Find the cells and give the type of each one.
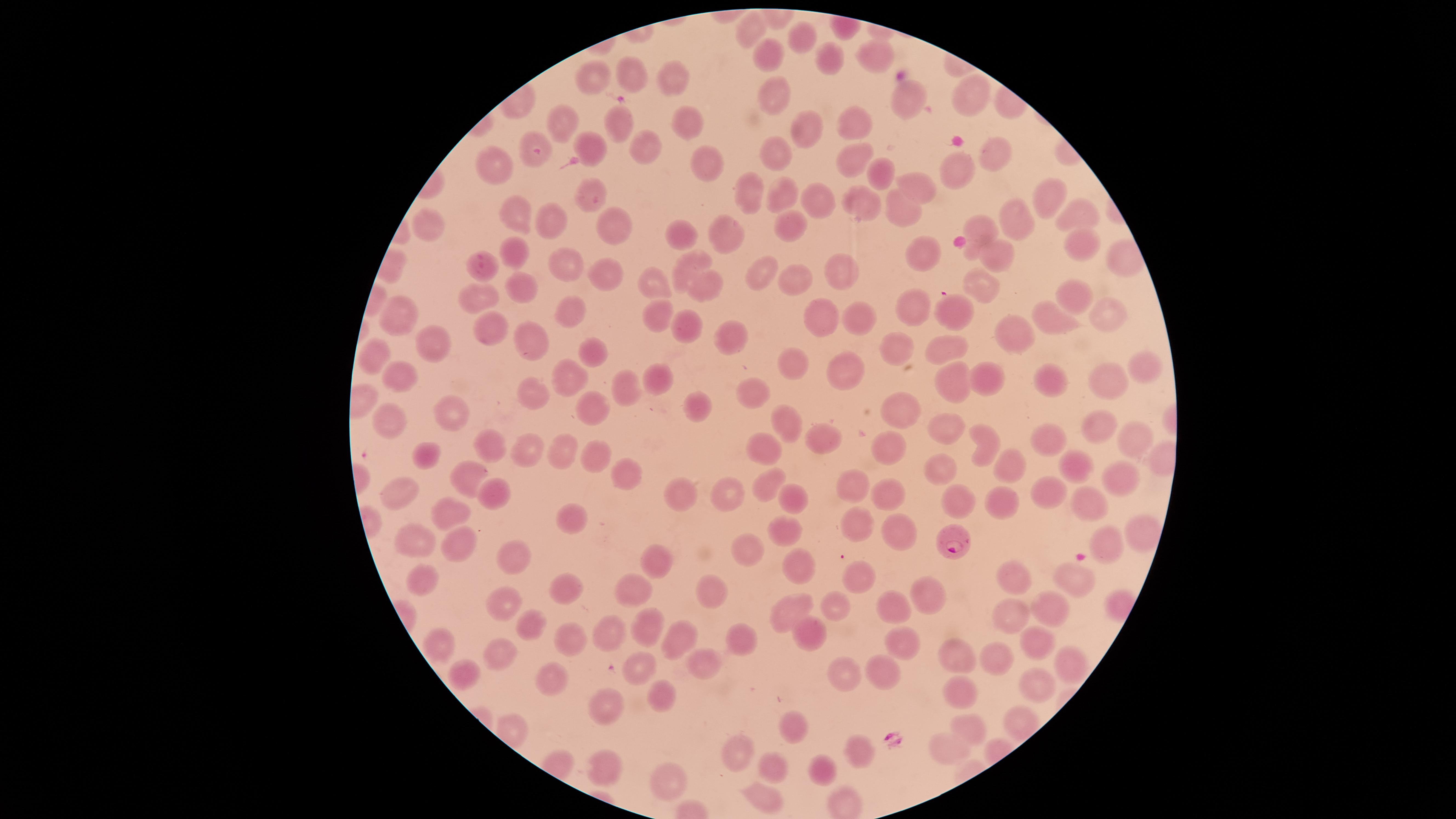

Approximate marker points as {x, y} in pixels.
Parasitized RBCs: {484, 267}, {953, 537}.
Uninfected RBCs: {752, 26}, {804, 40}, {773, 55}, {874, 55}, {829, 58}, {631, 75}, {671, 75}, {591, 77}, {774, 95}, {968, 98}, {905, 102}, {684, 118}, {564, 119}, {856, 123}, {621, 127}, {807, 130}, {531, 142}, {585, 147}, {649, 150}, {774, 153}, {990, 153}, {854, 158}, {709, 163}, {493, 166}, {876, 173}, {959, 175}, {917, 188}, {751, 194}, {1051, 194}, {591, 195}, {781, 198}, {813, 200}, {858, 200}, {900, 211}, {519, 214}, {551, 215}, {1074, 217}, {1014, 218}, {790, 222}, {428, 225}, {980, 226}, {616, 229}, {683, 230}, {723, 237}, {1077, 248}, {518, 249}, {930, 252}, {994, 254}, {560, 265}, {686, 266}, {835, 272}, {762, 274}, {606, 278}, {796, 282}, {525, 286}, {655, 286}, {982, 286}, {702, 287}, {1074, 293}, {480, 296}, {916, 308}, {566, 309}, {952, 311}, {396, 317}, {659, 317}, {818, 317}, {1110, 318}, {865, 324}, {1053, 326}, {492, 330}, {687, 330}, {1017, 332}, {727, 338}, {534, 340}, {894, 345}, {440, 347}, {947, 351}, {594, 352}, {370, 358}, {796, 362}, {848, 367}, {1144, 369}, {400, 376}, {570, 380}, {661, 381}, {984, 381}, {1047, 381}, {1111, 382}, {948, 387}, {535, 394}, {628, 395}, {752, 396}, {456, 406}, {699, 406}, {902, 407}, {397, 412}, {594, 414}, {787, 423}, {1103, 425}, {949, 427}, {825, 436}, {1050, 439}, {495, 442}, {1134, 442}, {989, 445}, {889, 448}, {766, 449}, {530, 452}, {559, 454}, {428, 457}, {590, 460}, {937, 463}, {1009, 463}, {1081, 464}, {1121, 475}, {631, 477}, {473, 480}, {763, 484}, {855, 487}, {402, 488}, {726, 490}, {887, 490}, {1048, 491}, {494, 492}, {679, 496}, {1083, 498}, {787, 499}, {956, 502}, {1000, 506}, {444, 513}, {567, 519}, {857, 525}, {784, 526}, {1138, 527}, {899, 530}, {1110, 541}, {415, 546}, {459, 546}, {753, 551}, {661, 558}, {514, 560}, {799, 567}, {857, 576}, {1021, 576}, {1081, 580}, {427, 581}, {563, 588}, {635, 589}, {710, 592}, {925, 595}, {503, 600}, {834, 606}, {893, 608}, {783, 611}, {1009, 611}, {1054, 612}, {648, 623}, {530, 627}, {608, 628}, {807, 634}, {682, 639}, {742, 639}, {1036, 640}, {577, 641}, {438, 643}, {901, 643}, {952, 654}, {505, 658}, {1000, 659}, {1068, 662}, {705, 663}, {641, 667}, {470, 673}, {883, 674}, {843, 678}, {552, 679}, {1041, 682}, {656, 693}, {961, 694}, {612, 704}, {1017, 721}, {973, 729}, {796, 732}, {944, 750}, {859, 751}, {733, 753}, {602, 768}, {774, 770}, {823, 771}, {663, 778}, {762, 800}.
No WBCs identified.

Giemsa stain. Image is 1456×819 pixels. Circular visible region. Species: Plasmodium falciparum. Thin blood smear. One field of view of the specimen. Photographed with a smartphone camera through the microscope eyepiece.